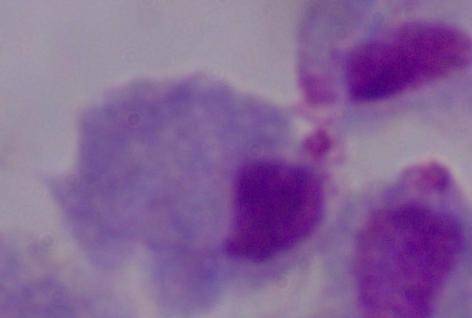

Summary:
  - Identification: trichomonad
  - Modality: micrograph
  - Magnification: 1000x